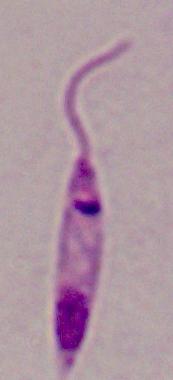
A Leishmania parasite is shown. Captured at 1000x magnification. Micrograph.